Outline each blood parasite and name the species.
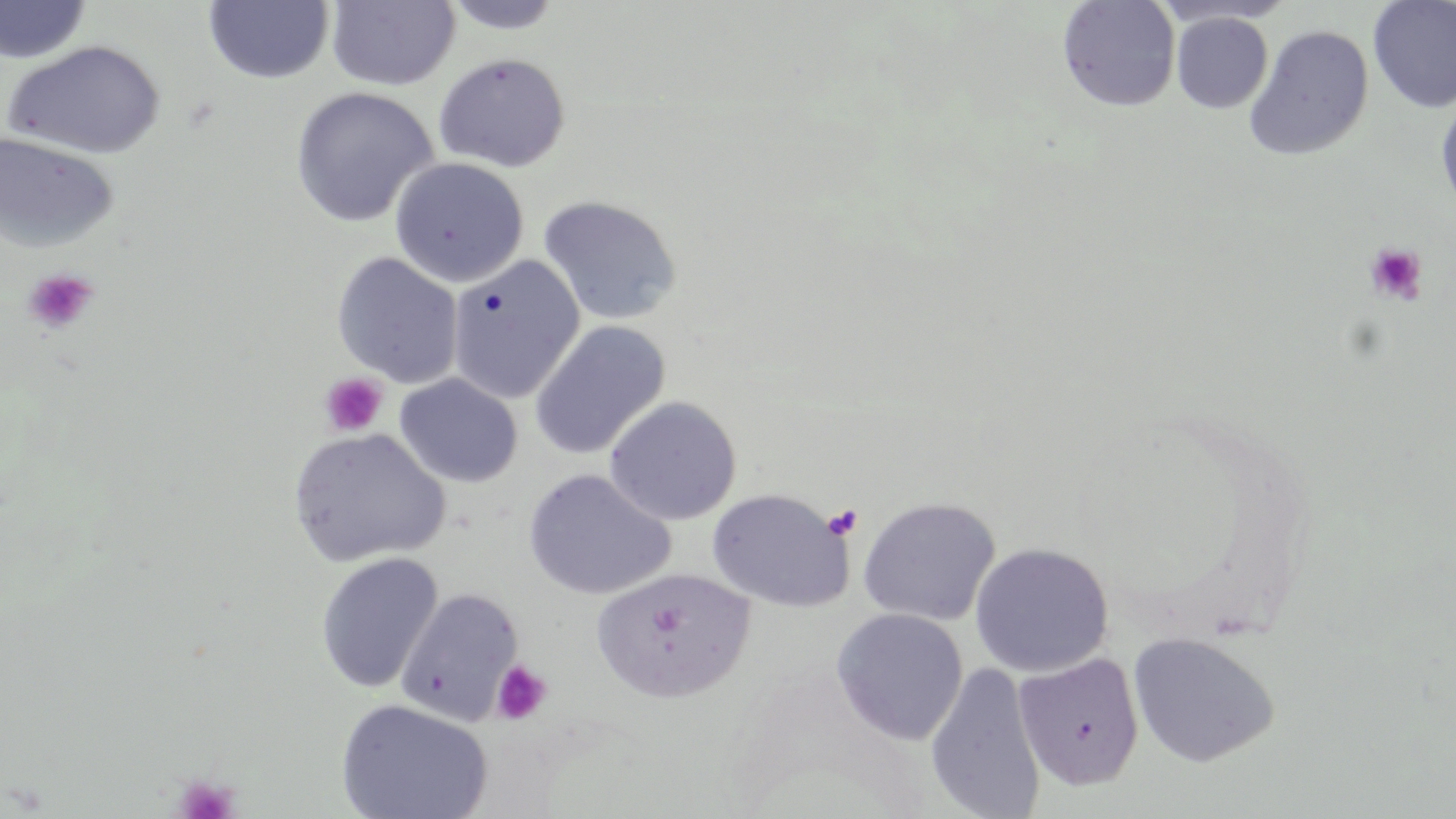
No blood parasites observed.

slide-level diagnosis = negative for blood parasites
field of view = single
preparation = thin blood film
stain = May-Grünwald-Giemsa
platelet locations = approximate bounding boxes as named x1/y1/x2/y2 corners in pixels: (x1=1363, y1=242, x2=1429, y2=306), (x1=22, y1=268, x2=99, y2=335), (x1=320, y1=372, x2=388, y2=437), (x1=822, y1=504, x2=863, y2=540), (x1=490, y1=660, x2=552, y2=725), (x1=172, y1=773, x2=240, y2=819)
magnification = 1000x
uninfected red blood cell locations = approximate bounding boxes as named x1/y1/x2/y2 corners in pixels: (x1=326, y1=0, x2=461, y2=91), (x1=1367, y1=0, x2=1456, y2=114), (x1=0, y1=1, x2=93, y2=64), (x1=202, y1=1, x2=335, y2=84), (x1=439, y1=1, x2=568, y2=35), (x1=1056, y1=1, x2=1181, y2=113), (x1=1170, y1=12, x2=1274, y2=113), (x1=1243, y1=24, x2=1375, y2=161), (x1=3, y1=40, x2=167, y2=159), (x1=433, y1=52, x2=571, y2=172), (x1=290, y1=86, x2=440, y2=228), (x1=1434, y1=90, x2=1456, y2=218), (x1=0, y1=132, x2=120, y2=253), (x1=389, y1=157, x2=529, y2=287), (x1=537, y1=194, x2=682, y2=327), (x1=331, y1=252, x2=464, y2=388), (x1=448, y1=255, x2=584, y2=403), (x1=528, y1=320, x2=671, y2=459), (x1=393, y1=373, x2=522, y2=488), (x1=603, y1=395, x2=742, y2=525), (x1=287, y1=427, x2=449, y2=567), (x1=522, y1=469, x2=675, y2=599), (x1=707, y1=488, x2=853, y2=612), (x1=857, y1=495, x2=1002, y2=627), (x1=969, y1=542, x2=1114, y2=677), (x1=315, y1=553, x2=443, y2=693), (x1=591, y1=568, x2=755, y2=703), (x1=394, y1=587, x2=524, y2=725), (x1=831, y1=608, x2=968, y2=745), (x1=1128, y1=630, x2=1280, y2=767), (x1=1013, y1=653, x2=1144, y2=790), (x1=924, y1=662, x2=1047, y2=819), (x1=335, y1=698, x2=493, y2=819)
modality = optical microscopy
image size = 1456×819 pixels